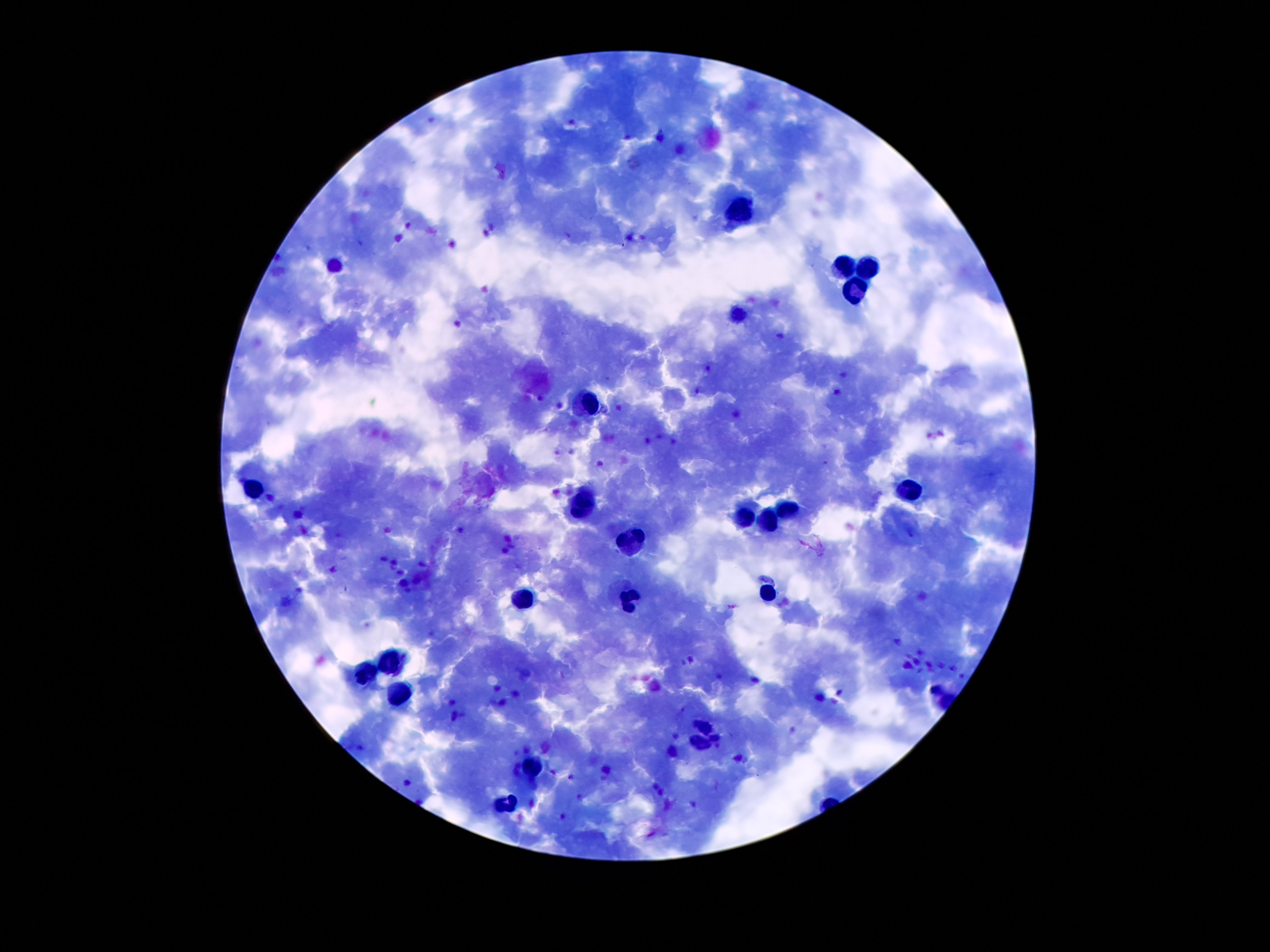
coordinate format = approximate object centers, in pixels from the top-left corner
leukocyte locations = (x=738, y=210), (x=843, y=267), (x=331, y=268), (x=872, y=270), (x=855, y=292), (x=736, y=311), (x=585, y=401), (x=250, y=487), (x=911, y=490), (x=582, y=505), (x=785, y=509), (x=744, y=516), (x=771, y=521), (x=632, y=542), (x=769, y=593), (x=522, y=596), (x=632, y=600), (x=387, y=661), (x=364, y=674), (x=397, y=696), (x=704, y=725), (x=701, y=743), (x=533, y=764), (x=504, y=805)
Plasmodium parasite locations = (x=461, y=530), (x=572, y=776)
stain = Giemsa
capture = smartphone through the microscope eyepiece
image size = 1270×952 pixels
magnification = 100x
preparation = thick peripheral-blood smear
patient malaria status = positive for Plasmodium falciparum
field of view = single